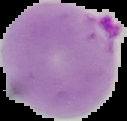

result = Plasmodium parasites identified
image size = 127×121 pixels
image type = segmented cell region with the area outside set to black
preparation = thin blood film